Identify the parasite.
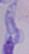

This is a trypanosome.

Captured at 1000x magnification. Photomicrograph.